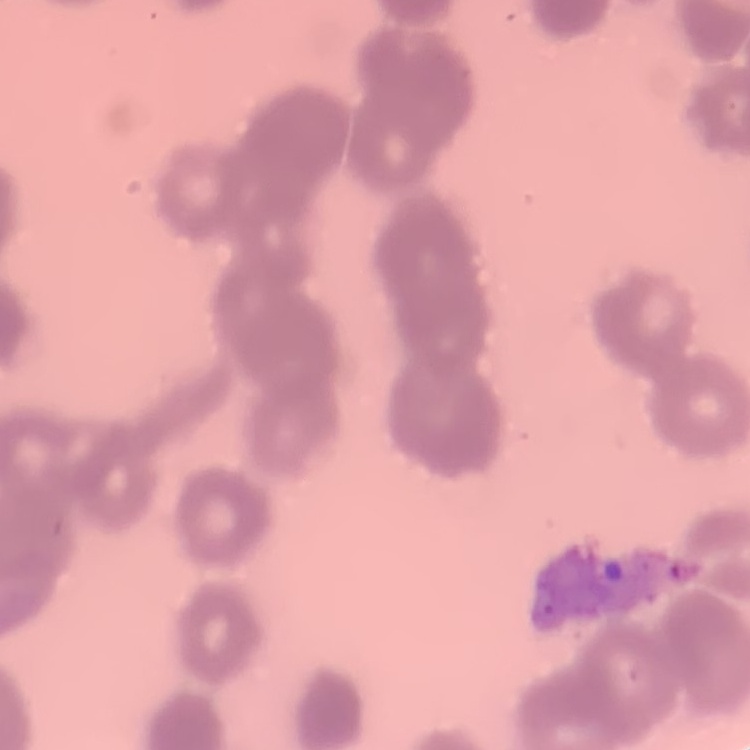
red blood cell morphology = rouleaux formation
preparation = thin peripheral smear
stain = Field's or Giemsa
image type = one tile cut from a larger photomicrograph